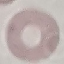
Malaria status: uninfected. Thin blood film. Giemsa stain. Acquired by smartphone through the microscope eyepiece. Automatically extracted cell patch, resized to 64 × 64 pixels.